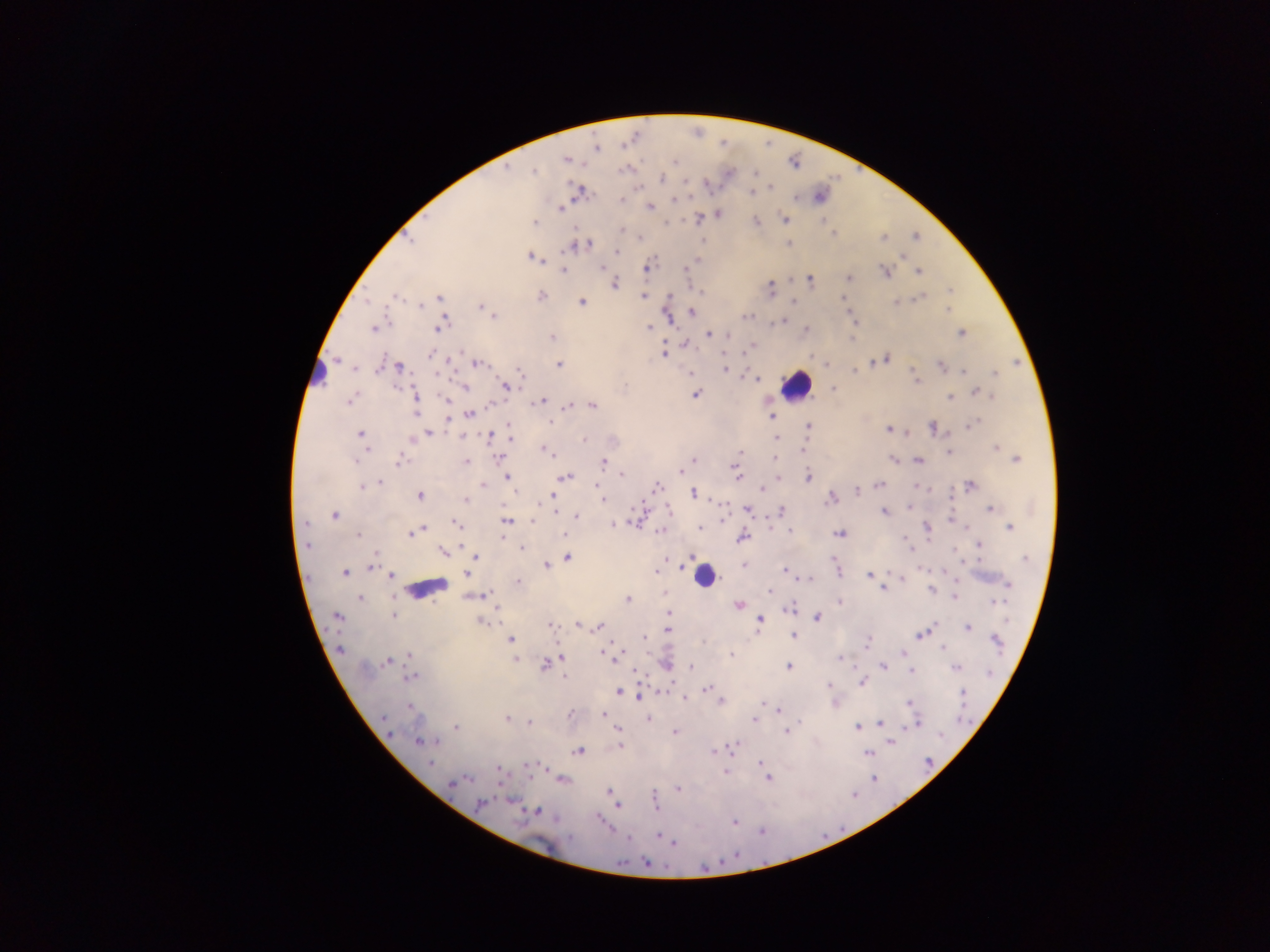

Approximate centers as (x, y) in pixels.
Summary:
  - Malaria parasite locations: (596, 148), (567, 158), (675, 161), (506, 168), (534, 170), (661, 178), (770, 186), (578, 191), (751, 192), (622, 201), (560, 207), (649, 207), (719, 213), (698, 218), (784, 220), (756, 221), (535, 222), (834, 233), (915, 236), (639, 237), (883, 238), (788, 242), (578, 245), (617, 251), (902, 255), (531, 256), (695, 259), (602, 267), (646, 268), (563, 270), (883, 272), (918, 272), (848, 278), (809, 279), (614, 284), (770, 288), (949, 290), (541, 295), (396, 296), (642, 296), (921, 297), (440, 298), (843, 298), (668, 299), (792, 301), (895, 301), (581, 302), (422, 305), (481, 306), (948, 310), (691, 311), (746, 315), (494, 316), (666, 317), (782, 320), (854, 321), (441, 324), (373, 327), (648, 328), (804, 332), (961, 332), (708, 335), (851, 336), (551, 337), (685, 344), (751, 347), (727, 351), (662, 352), (431, 354), (885, 359), (337, 360), (476, 363), (559, 364), (380, 365), (941, 365), (397, 366), (724, 366), (518, 370), (725, 370), (853, 370), (963, 370), (689, 373), (995, 374), (756, 377), (915, 378), (504, 385), (464, 386), (833, 388), (975, 392), (695, 394), (414, 396), (949, 397), (350, 400), (447, 400), (542, 401), (489, 405), (570, 406), (591, 406), (469, 414), (772, 417), (551, 423), (508, 425), (970, 425), (808, 426), (932, 429), (889, 430), (906, 431), (428, 433), (361, 434), (489, 435), (509, 435), (775, 438), (410, 439), (583, 439), (996, 447), (366, 448), (804, 448), (1004, 449), (545, 450), (949, 451), (773, 457), (499, 458), (1016, 458), (694, 459), (893, 459), (918, 460), (399, 461), (466, 462), (603, 463), (735, 468), (680, 471), (622, 473), (736, 475), (507, 477), (565, 477), (777, 477), (808, 477), (378, 482), (970, 484), (360, 485), (481, 485), (878, 485), (656, 487), (918, 487), (598, 488), (763, 488), (856, 491), (692, 493), (419, 495), (553, 495), (830, 497), (465, 499), (603, 500), (908, 506), (668, 508), (747, 509), (781, 509), (988, 509), (885, 512), (557, 513), (334, 516), (575, 516), (949, 518), (532, 519), (506, 521), (304, 523), (455, 523), (613, 524), (768, 525), (700, 527), (926, 527), (1009, 527), (421, 529), (661, 530), (790, 530), (408, 533), (840, 534), (358, 535), (502, 536), (565, 536), (740, 537), (903, 537), (306, 545), (979, 545), (522, 548), (443, 551), (376, 555), (690, 556), (475, 557), (568, 558), (1025, 559), (545, 565), (743, 565), (369, 567), (836, 569), (657, 570), (784, 570), (466, 571), (345, 573), (868, 574), (392, 576), (808, 578), (902, 578), (517, 582), (955, 582), (1007, 584), (884, 588), (932, 589), (769, 591), (663, 593), (478, 595), (954, 597), (360, 598), (627, 599), (839, 601), (993, 601), (739, 604), (790, 608), (497, 610), (669, 612), (392, 614), (336, 617), (816, 617), (481, 620), (759, 620), (550, 624), (578, 624), (600, 626), (967, 627), (666, 631), (920, 634), (794, 635), (645, 637), (510, 639), (996, 640), (866, 642), (941, 648), (339, 649), (902, 652), (411, 654), (601, 654), (731, 654), (616, 657), (560, 658), (839, 658), (386, 660), (514, 660), (548, 661), (543, 664), (666, 664), (691, 666), (788, 666), (882, 666), (956, 668), (634, 671), (911, 671), (411, 676), (565, 677), (861, 682), (828, 686), (706, 689), (618, 692), (962, 693), (638, 696), (684, 697), (721, 702), (836, 703), (909, 703), (410, 707), (778, 710), (603, 713), (569, 714), (647, 718), (506, 719), (755, 719), (528, 722), (879, 724), (914, 724), (858, 726), (456, 727), (617, 729), (787, 731), (675, 732), (419, 740), (427, 741), (891, 741), (620, 745), (731, 748), (578, 751), (712, 751), (869, 753), (759, 762), (430, 763), (528, 765), (497, 767), (725, 772), (767, 777), (562, 779), (874, 779), (453, 783), (677, 788), (608, 790), (511, 800), (480, 804), (616, 806), (655, 806), (537, 811), (598, 819), (734, 820), (657, 835), (674, 843)
  - Leukocyte locations: (317, 375), (797, 385), (703, 575), (426, 589)
  - Image size: 1270×952 pixels
  - Country: Ghana
  - Preparation: thick blood film
  - Field of view: single
  - Capture: mobile-phone photograph through a microscope